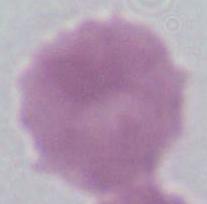

Photomicrograph. An erythrocyte is seen. 1000x magnification.